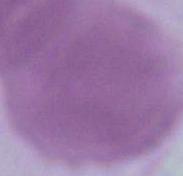

modality = photomicrograph
magnification = 1000x
identification = erythrocyte